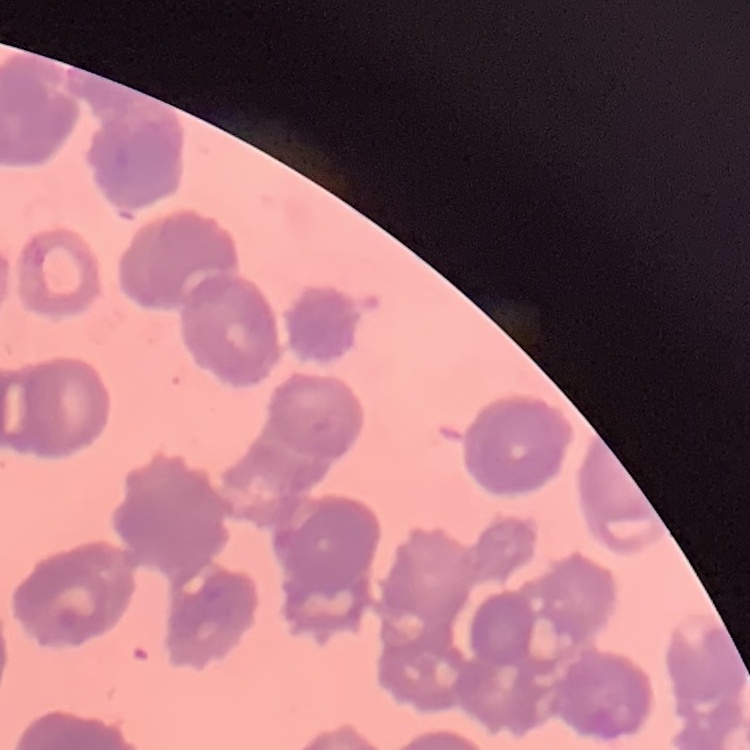
Summary:
  - Erythrocyte morphology: rouleaux formation
  - Preparation: thin blood smear
  - Stain: Field's or Giemsa
  - Image type: one tile cut from a larger photomicrograph